Report the malaria status of this cell.
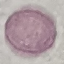

Uninfected.

Automatically extracted cell patch, resized to 64 × 64 pixels. Thin blood smear. Giemsa stain. Acquired by smartphone through the microscope eyepiece.